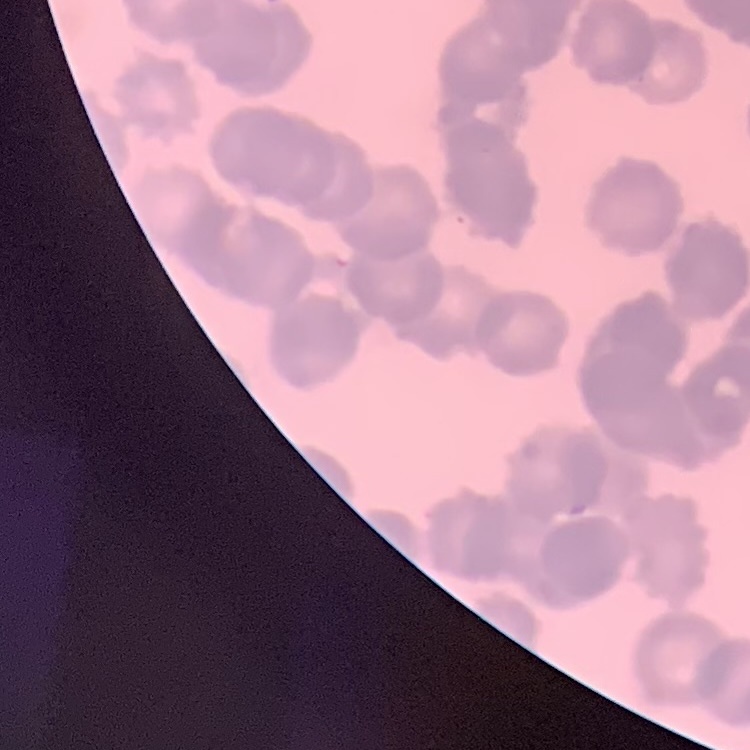

red blood cell morphology = rouleaux formation
stain = Field's or Giemsa
image type = one tile cut from a larger photomicrograph
preparation = thin peripheral smear